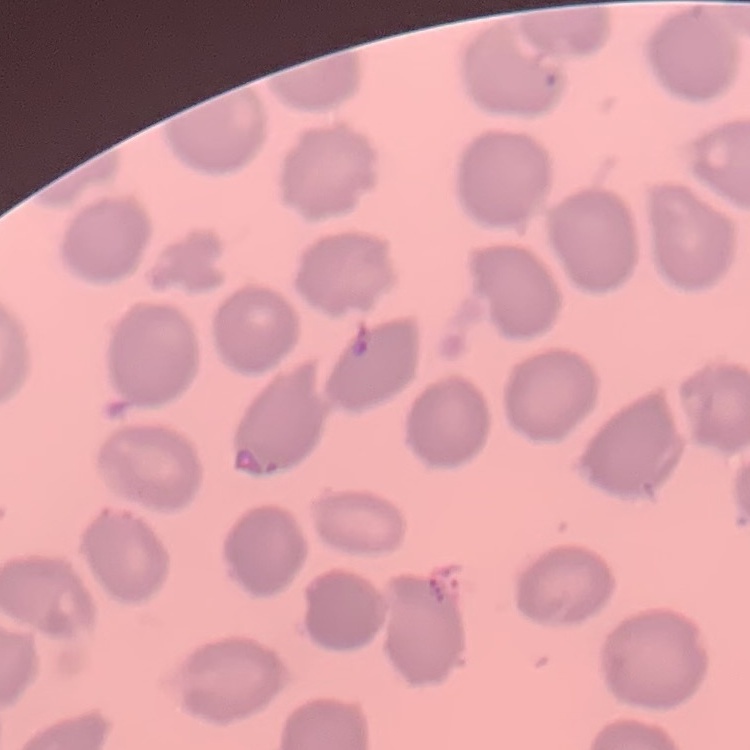
erythrocyte_morphology: no rouleaux formation
stain: Field's or Giemsa
preparation: thin peripheral smear
image_type: one tile cut from a larger photomicrograph